Describe the morphology of the red blood cells.
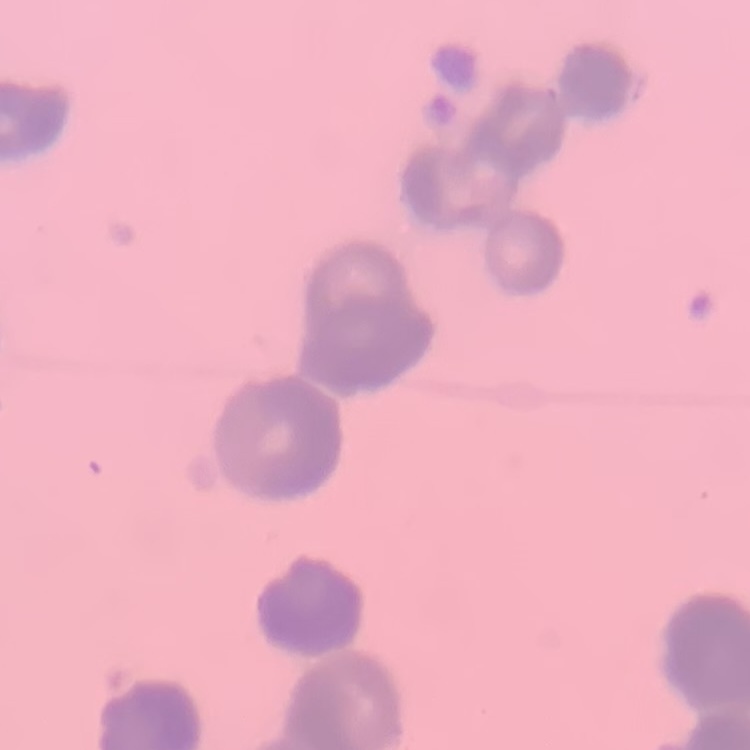

They show rouleaux formation.

stain = Field's or Giemsa
preparation = thin peripheral smear
image type = one tile cut from a larger photomicrograph